Outline each blood parasite and name the species.
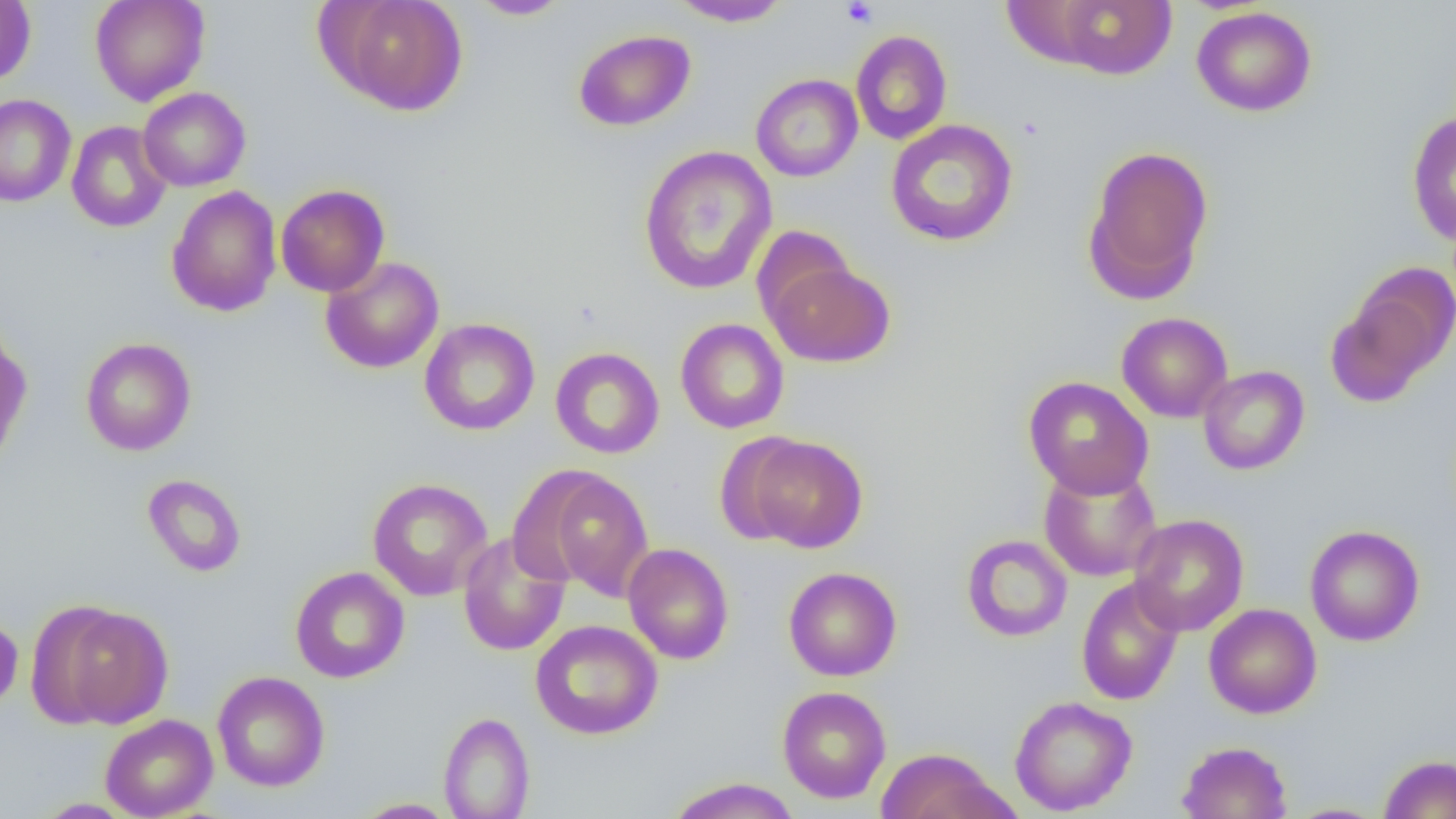

No blood parasites observed.

Approximate bounding boxes as (x1,y1)-(x2,y2) corner pairs in pixels. Platelet locations: (841,1)-(878,28). Uninfected red blood cell locations: (89,0)-(210,105), (327,0)-(469,117), (467,0)-(572,20), (668,0)-(793,27), (1052,0)-(1176,79), (0,1)-(36,85), (1191,7)-(1317,116), (573,29)-(696,131), (851,30)-(952,145), (750,74)-(863,182), (138,87)-(251,192), (0,94)-(76,208), (1406,110)-(1456,248), (885,119)-(1019,247), (67,121)-(172,233), (1083,144)-(1214,303), (638,145)-(778,296), (275,184)-(390,297), (166,185)-(282,317), (750,225)-(857,326), (320,256)-(444,374), (764,258)-(896,368), (1327,273)-(1452,405), (1116,312)-(1233,423), (419,318)-(540,436), (675,318)-(789,434), (0,331)-(32,466), (80,338)-(196,456), (550,347)-(665,459), (1198,365)-(1309,475), (1023,376)-(1153,498), (744,434)-(868,553), (1038,462)-(1162,582), (531,467)-(655,599), (142,473)-(247,577), (367,477)-(493,601), (1128,513)-(1249,636), (1304,524)-(1425,646), (457,532)-(570,656), (961,534)-(1072,642), (623,543)-(734,664), (290,566)-(409,684), (784,566)-(902,682), (1076,576)-(1184,706), (1204,603)-(1321,719), (54,604)-(173,727), (0,615)-(23,713), (531,619)-(663,740), (212,671)-(329,792), (777,686)-(891,803), (1009,695)-(1138,816), (438,711)-(535,818), (100,714)-(218,819), (1177,740)-(1291,819), (874,747)-(1014,819), (1379,754)-(1456,818), (667,777)-(801,819), (352,798)-(461,818), (1284,803)-(1389,819). Slide-level diagnosis: no evidence of blood parasites. Captured at 1000x magnification. One field of a larger specimen. Thin blood film. Optical microscopy. Image is 1456×819 pixels.